State which cell type is depicted.
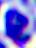
A leukocyte.

Summary:
  - Modality: photomicrograph
  - Magnification: 400x